Locate every blood parasite and identify its species.
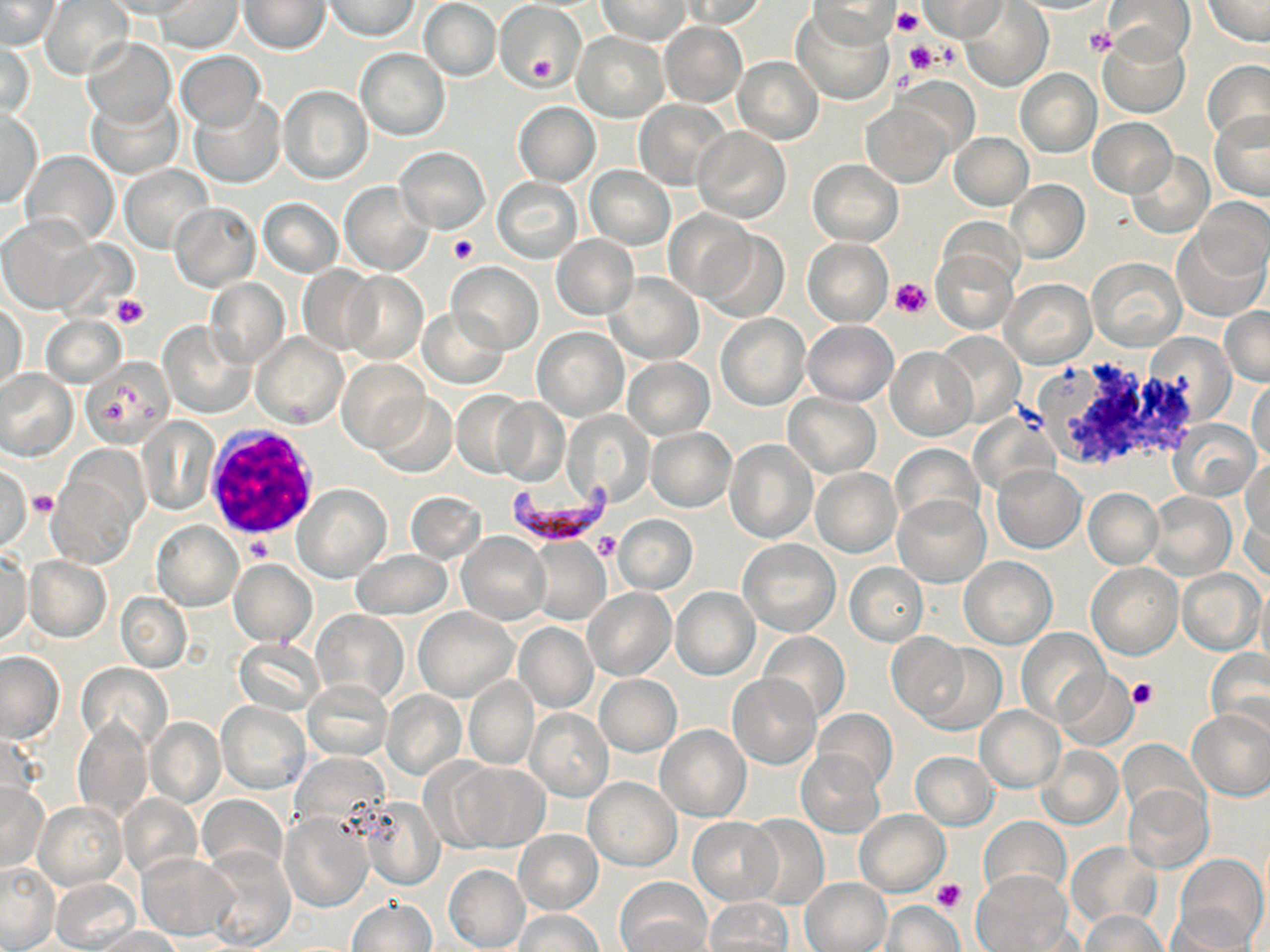
Approximate bounding boxes as [x1, y1, x2, y2] in pixels.
Plasmodium falciparum-infected red blood cells: [504, 481, 620, 540].
No Plasmodium ovale, Plasmodium malariae, Plasmodium vivax, Babesia divergens, or Trypanosoma brucei observed.

White blood cell locations: [203, 427, 319, 545]. Platelet locations: [891, 5, 924, 37], [897, 12, 933, 50], [1084, 26, 1117, 59], [934, 38, 962, 69], [904, 41, 938, 73], [527, 52, 558, 84], [448, 234, 478, 265], [890, 277, 933, 318], [111, 294, 149, 330], [1013, 400, 1050, 433], [29, 489, 56, 518], [592, 532, 621, 560], [247, 537, 272, 561], [1127, 679, 1158, 709], [930, 878, 967, 912]. Uninfected red blood cell locations: [42, 0, 134, 80], [102, 0, 199, 18], [324, 0, 419, 41], [598, 0, 692, 42], [678, 0, 769, 28], [919, 0, 1009, 40], [1201, 0, 1269, 46], [1, 1, 61, 50], [156, 1, 240, 54], [239, 1, 330, 54], [420, 1, 501, 82], [494, 1, 587, 91], [805, 1, 900, 48], [1105, 1, 1194, 65], [960, 2, 1052, 91], [793, 7, 895, 105], [659, 22, 746, 107], [574, 33, 668, 121], [1099, 33, 1189, 118], [81, 37, 176, 127], [1, 41, 35, 120], [356, 48, 450, 140], [176, 51, 265, 130], [734, 56, 824, 143], [1201, 59, 1270, 149], [1015, 69, 1101, 157], [894, 74, 977, 159], [278, 86, 372, 185], [86, 91, 183, 180], [191, 97, 285, 189], [634, 100, 732, 192], [513, 102, 600, 186], [862, 102, 953, 188], [0, 109, 42, 208], [1208, 110, 1270, 201], [1089, 119, 1176, 196], [691, 127, 789, 223], [949, 132, 1032, 210], [394, 146, 491, 233], [21, 150, 119, 248], [1127, 153, 1213, 238], [807, 159, 903, 246], [120, 165, 213, 253], [586, 166, 675, 250], [492, 177, 583, 263], [1007, 180, 1088, 262], [340, 181, 432, 275], [259, 198, 343, 278], [1194, 198, 1269, 280], [169, 201, 259, 292], [665, 210, 751, 302], [937, 216, 1022, 294], [0, 219, 99, 313], [1174, 227, 1268, 322], [699, 229, 789, 323], [552, 235, 639, 319], [802, 238, 893, 326], [931, 249, 1017, 334], [1088, 259, 1185, 351], [448, 262, 543, 353], [297, 265, 379, 355], [342, 272, 428, 365], [607, 273, 702, 364], [1002, 278, 1096, 368], [205, 279, 289, 368], [1, 301, 27, 390], [1220, 307, 1269, 386], [419, 308, 508, 388], [717, 313, 810, 410], [41, 314, 125, 387], [160, 321, 254, 417], [804, 321, 897, 406], [533, 327, 627, 420], [935, 332, 1024, 426], [253, 333, 347, 428], [1144, 333, 1237, 425], [886, 346, 977, 441], [80, 358, 176, 446], [624, 358, 713, 440], [339, 359, 427, 450], [0, 370, 77, 462], [1248, 375, 1270, 464], [453, 390, 532, 477], [373, 394, 456, 478], [785, 394, 880, 477], [491, 397, 569, 487], [564, 410, 654, 508], [971, 414, 1059, 499], [138, 418, 218, 513], [1169, 420, 1261, 501], [646, 428, 735, 511], [724, 439, 817, 542], [890, 444, 983, 530], [49, 455, 144, 563], [1242, 457, 1270, 546], [991, 465, 1086, 553], [0, 467, 31, 551], [811, 467, 902, 557], [294, 485, 391, 582], [1083, 488, 1163, 569], [405, 491, 487, 564], [1147, 492, 1236, 581], [892, 495, 990, 588], [1242, 501, 1269, 584], [613, 514, 696, 594], [153, 522, 242, 611], [457, 532, 550, 625], [525, 538, 609, 626], [737, 539, 841, 637], [352, 549, 451, 620], [1, 552, 33, 646], [25, 556, 111, 642], [960, 556, 1057, 648], [229, 560, 316, 646], [844, 562, 928, 646], [1088, 563, 1182, 659], [1178, 567, 1266, 655], [1255, 580, 1270, 676], [583, 588, 675, 680], [671, 588, 759, 680], [117, 593, 191, 672], [415, 609, 518, 702], [314, 610, 406, 701], [514, 623, 597, 713], [1017, 628, 1110, 726], [758, 631, 850, 725], [888, 632, 969, 720], [234, 639, 322, 716], [916, 642, 1006, 735], [1206, 649, 1270, 740], [0, 653, 63, 743], [76, 663, 173, 752], [1050, 669, 1136, 751], [729, 674, 819, 769], [595, 675, 681, 756], [463, 677, 538, 771], [302, 679, 391, 760], [382, 690, 466, 780], [217, 702, 310, 794], [976, 706, 1065, 792], [810, 707, 897, 793], [1187, 708, 1270, 800], [526, 709, 614, 801], [73, 718, 153, 824], [146, 718, 224, 808], [656, 725, 750, 822], [1117, 739, 1207, 821], [1035, 745, 1122, 830], [797, 751, 884, 837], [910, 752, 998, 830], [450, 763, 548, 852], [582, 776, 682, 869], [0, 783, 48, 872], [1124, 785, 1212, 871], [118, 795, 202, 881], [197, 795, 287, 877], [360, 798, 444, 889], [35, 801, 127, 890], [854, 809, 949, 896], [281, 812, 373, 912], [742, 815, 828, 908], [980, 816, 1069, 900], [688, 817, 781, 905], [514, 830, 602, 913], [1067, 842, 1160, 931], [200, 847, 295, 951], [136, 852, 234, 939], [1175, 853, 1267, 950], [0, 863, 59, 950], [444, 865, 530, 952], [970, 869, 1075, 952], [51, 877, 142, 952], [801, 877, 891, 952], [616, 878, 712, 952], [706, 898, 793, 951], [348, 899, 434, 951], [881, 899, 962, 951], [1168, 906, 1261, 952], [514, 908, 603, 952], [1078, 909, 1169, 952], [96, 926, 183, 951]. Slide-level diagnosis: Plasmodium falciparum. Image is 1270×952 pixels. May-Grünwald-Giemsa-stained preparation. Optical microscopy. Captured at 1000x magnification. Thin blood film. Single field of view.